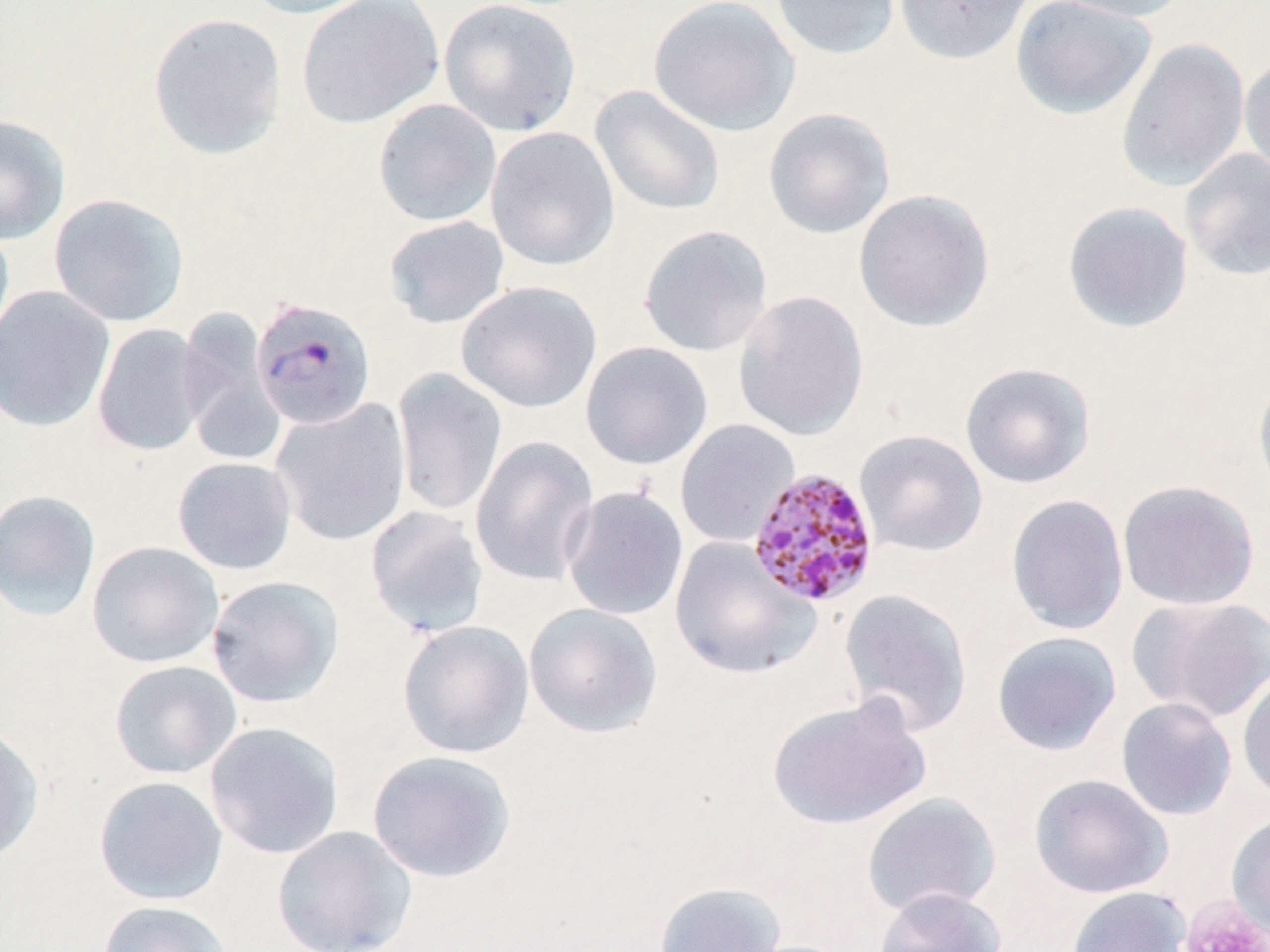
slide-level diagnosis = Plasmodium malariae
preparation = thin blood film
platelet locations = approximate bounding boxes as named x1/y1/x2/y2 corners in pixels: (x1=1179, y1=896, x2=1269, y2=952)
stain = May-Grünwald-Giemsa
field of view = one of a larger specimen
Plasmodium malariae-infected red blood cell locations = approximate bounding boxes as named x1/y1/x2/y2 corners in pixels: (x1=251, y1=297, x2=377, y2=430), (x1=751, y1=468, x2=885, y2=610)
modality = optical microscopy
image size = 1270×952 pixels
magnification = 1000x
uninfected red blood cell locations = approximate bounding boxes as named x1/y1/x2/y2 corners in pixels: (x1=240, y1=0, x2=383, y2=20), (x1=296, y1=0, x2=444, y2=129), (x1=439, y1=0, x2=582, y2=137), (x1=648, y1=0, x2=800, y2=136), (x1=770, y1=0, x2=901, y2=60), (x1=894, y1=0, x2=1034, y2=65), (x1=1010, y1=0, x2=1156, y2=120), (x1=1044, y1=0, x2=1190, y2=22), (x1=148, y1=12, x2=288, y2=160), (x1=1115, y1=37, x2=1250, y2=192), (x1=1239, y1=56, x2=1270, y2=184), (x1=590, y1=85, x2=727, y2=216), (x1=373, y1=98, x2=502, y2=227), (x1=763, y1=108, x2=896, y2=239), (x1=0, y1=114, x2=70, y2=245), (x1=485, y1=126, x2=619, y2=270), (x1=1179, y1=148, x2=1270, y2=282), (x1=854, y1=189, x2=996, y2=333), (x1=49, y1=193, x2=190, y2=327), (x1=1062, y1=200, x2=1194, y2=334), (x1=383, y1=215, x2=510, y2=329), (x1=0, y1=220, x2=15, y2=360), (x1=638, y1=225, x2=773, y2=357), (x1=457, y1=280, x2=602, y2=413), (x1=0, y1=286, x2=115, y2=433), (x1=733, y1=290, x2=869, y2=442), (x1=176, y1=307, x2=285, y2=464), (x1=92, y1=323, x2=208, y2=457), (x1=580, y1=341, x2=713, y2=471), (x1=960, y1=361, x2=1097, y2=489), (x1=391, y1=368, x2=508, y2=517), (x1=1253, y1=370, x2=1270, y2=501), (x1=271, y1=398, x2=411, y2=546), (x1=674, y1=418, x2=800, y2=548), (x1=855, y1=429, x2=988, y2=557), (x1=470, y1=435, x2=600, y2=586), (x1=172, y1=456, x2=296, y2=576), (x1=1117, y1=479, x2=1260, y2=610), (x1=560, y1=486, x2=689, y2=621), (x1=0, y1=489, x2=102, y2=622), (x1=1006, y1=495, x2=1129, y2=636), (x1=365, y1=505, x2=490, y2=639), (x1=669, y1=537, x2=821, y2=680), (x1=86, y1=541, x2=225, y2=668), (x1=206, y1=575, x2=345, y2=708), (x1=838, y1=588, x2=974, y2=738), (x1=1128, y1=595, x2=1270, y2=724), (x1=523, y1=602, x2=664, y2=739), (x1=397, y1=620, x2=535, y2=759), (x1=991, y1=631, x2=1122, y2=757), (x1=109, y1=659, x2=242, y2=780), (x1=1238, y1=668, x2=1270, y2=803), (x1=766, y1=694, x2=931, y2=831), (x1=1116, y1=697, x2=1237, y2=821), (x1=203, y1=721, x2=345, y2=859), (x1=0, y1=723, x2=45, y2=864), (x1=366, y1=750, x2=517, y2=883), (x1=1029, y1=773, x2=1173, y2=899), (x1=94, y1=775, x2=228, y2=905), (x1=862, y1=792, x2=1001, y2=918), (x1=1227, y1=812, x2=1270, y2=938), (x1=271, y1=825, x2=417, y2=952), (x1=652, y1=881, x2=788, y2=952), (x1=873, y1=886, x2=1008, y2=952), (x1=1067, y1=886, x2=1191, y2=952), (x1=97, y1=899, x2=233, y2=952)